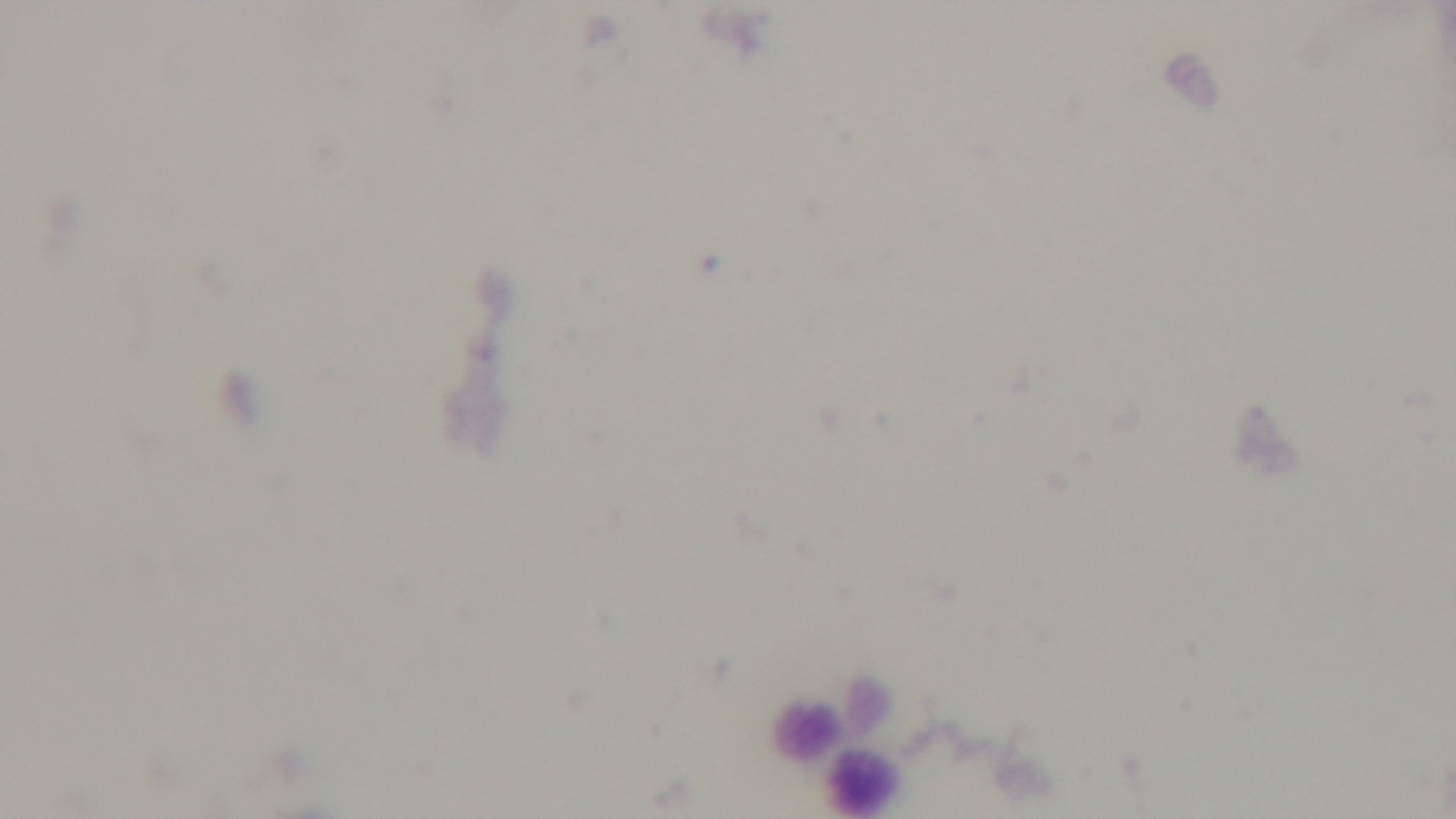

Photomicrograph. Captured with a mounted 4K digital camera. Malaria status: negative. Giemsa-stained. One field from the slide. Preparation: thick smear. Oil-immersion objective, 100x.